Locate every blood parasite and identify its species.
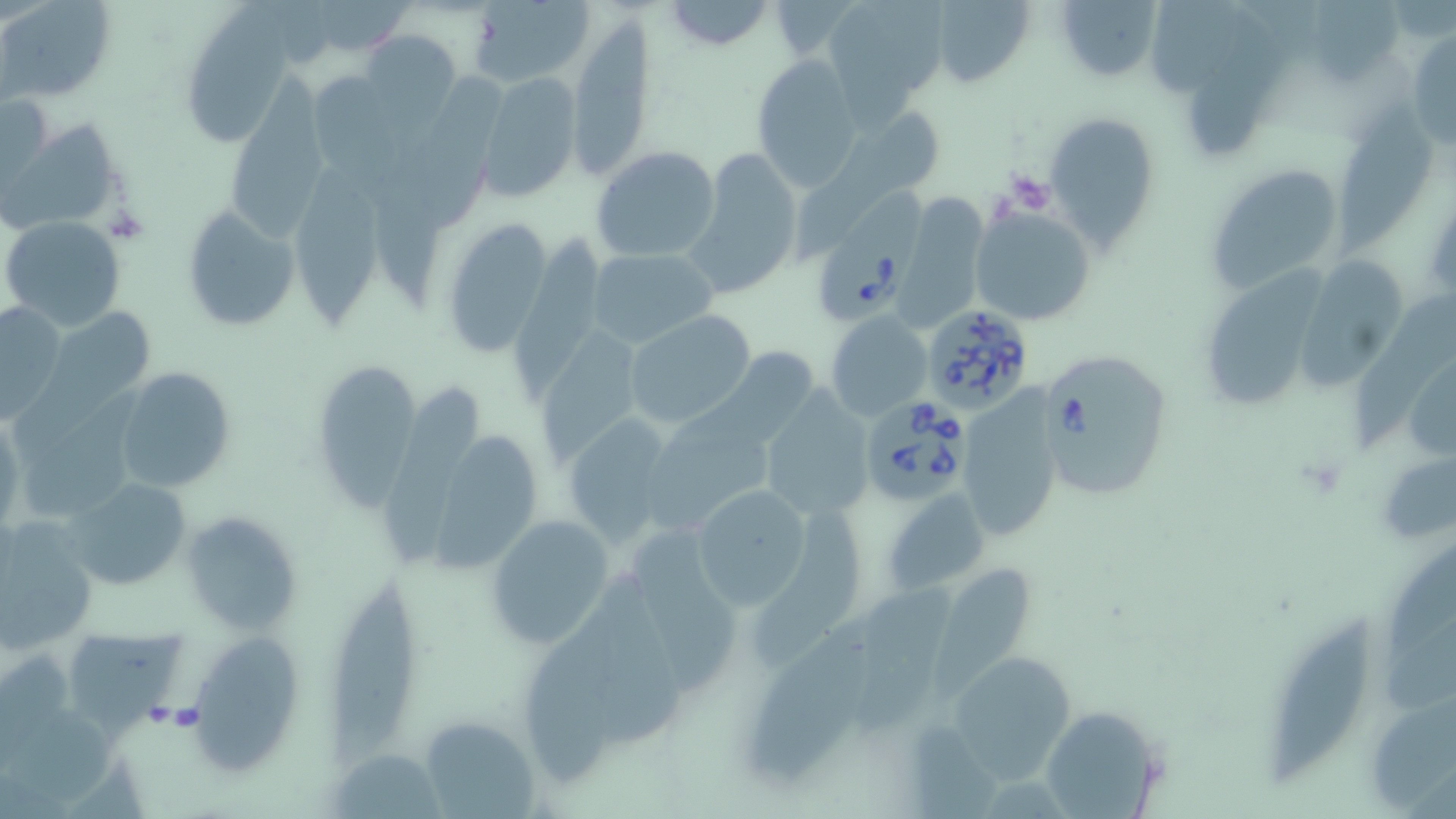

Approximate bounding boxes as [x1, y1, x2, y2] in pixels.
Babesia divergens-infected red blood cells: [818, 182, 924, 328], [919, 303, 1036, 416], [1038, 347, 1171, 500], [860, 395, 971, 508].
No Plasmodium falciparum, Plasmodium ovale, Plasmodium malariae, Plasmodium vivax, or Trypanosoma brucei observed.

Platelet locations: [1005, 171, 1053, 213], [165, 704, 203, 732]. Uninfected red blood cell locations: [3, 0, 115, 102], [472, 0, 593, 88], [925, 0, 1035, 86], [1054, 0, 1164, 85], [661, 1, 774, 50], [300, 2, 411, 58], [1144, 3, 1247, 94], [188, 4, 295, 151], [824, 4, 958, 140], [567, 15, 654, 180], [1190, 20, 1285, 153], [360, 30, 460, 129], [1407, 34, 1456, 149], [752, 58, 861, 192], [223, 66, 332, 249], [478, 70, 584, 202], [314, 72, 403, 202], [0, 91, 53, 192], [845, 105, 948, 200], [1045, 110, 1163, 251], [1337, 115, 1437, 252], [2, 117, 125, 237], [591, 146, 722, 262], [690, 149, 803, 295], [1205, 160, 1351, 295], [298, 169, 386, 326], [903, 194, 991, 322], [178, 203, 300, 335], [970, 206, 1097, 327], [1, 216, 127, 331], [440, 216, 552, 357], [509, 234, 602, 405], [587, 248, 718, 349], [1300, 255, 1403, 386], [1202, 268, 1329, 410], [1353, 297, 1456, 443], [1, 300, 68, 424], [43, 306, 156, 412], [827, 310, 932, 420], [623, 311, 757, 429], [543, 333, 636, 462], [307, 361, 420, 511], [112, 367, 234, 494], [389, 376, 475, 567], [956, 386, 1064, 543], [757, 387, 877, 525], [648, 409, 770, 530], [562, 412, 684, 546], [0, 414, 23, 534], [431, 429, 546, 573], [1375, 448, 1455, 550], [63, 475, 191, 591], [693, 484, 815, 610], [882, 489, 990, 596], [181, 506, 303, 637], [753, 507, 865, 666], [485, 512, 618, 650], [0, 515, 99, 654], [634, 530, 741, 690], [1391, 541, 1456, 659], [927, 567, 1032, 696], [601, 572, 686, 739], [330, 577, 418, 757], [850, 587, 959, 730], [526, 610, 628, 786], [748, 611, 875, 788], [1263, 613, 1374, 790], [66, 626, 188, 746], [186, 632, 304, 774], [955, 656, 1073, 783], [1038, 706, 1165, 816], [419, 714, 541, 818], [334, 748, 442, 816]. Slide-level diagnosis: Babesia divergens. Thin blood film. Optical microscopy. 1000x magnification. Image is 1456×819 pixels. May-Grünwald-Giemsa stain. One field of a larger specimen.